Locate every uninfected red blood cell.
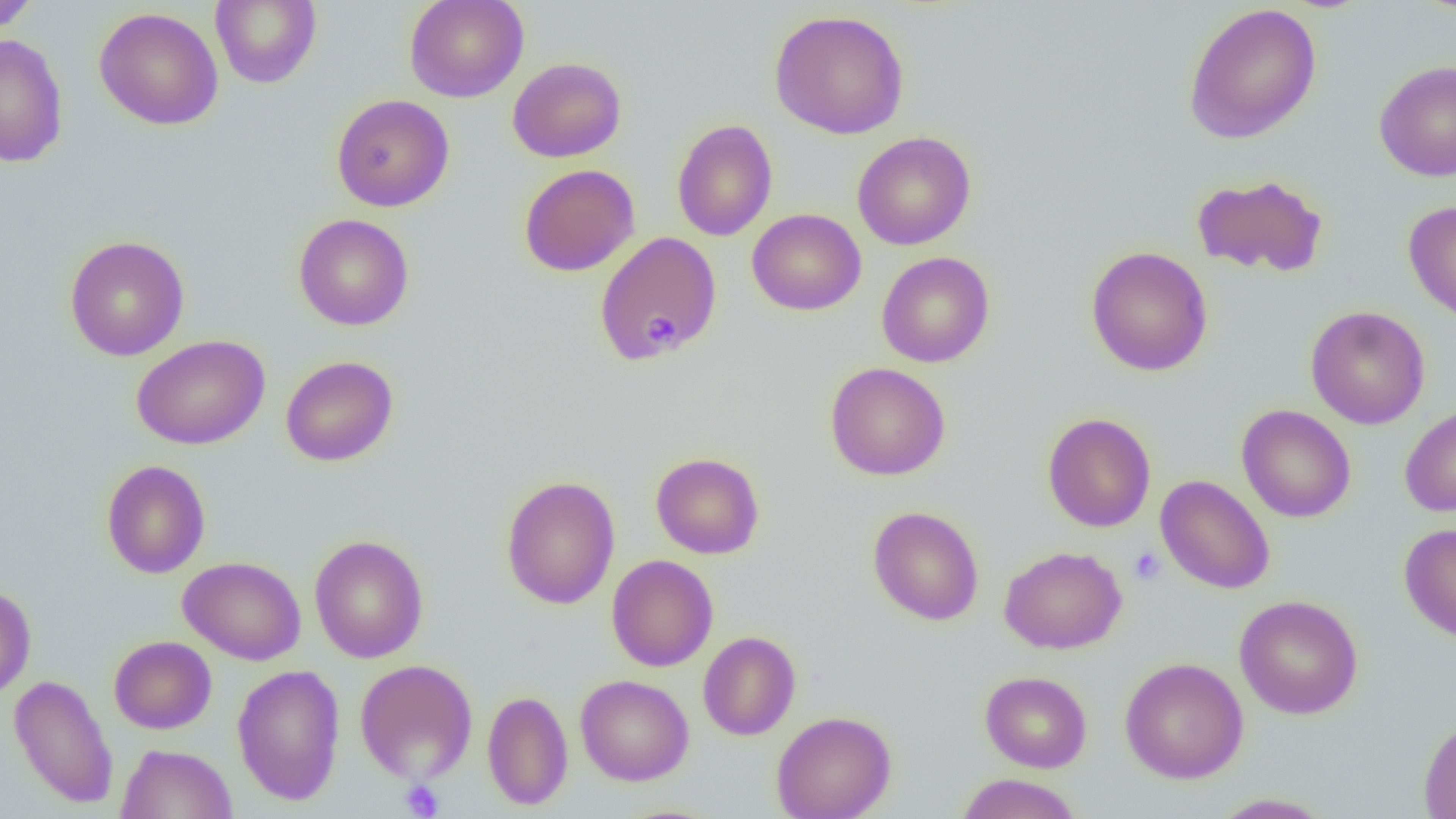
Approximate bounding boxes as [x1, y1, x2, y2] in pixels.
Uninfected red blood cells: [0, 0, 40, 34], [210, 0, 322, 88], [404, 0, 529, 102], [1414, 0, 1456, 16], [1183, 2, 1322, 144], [94, 7, 224, 131], [769, 9, 910, 139], [1, 34, 69, 167], [508, 57, 626, 163], [1374, 60, 1456, 182], [331, 95, 454, 212], [672, 119, 777, 241], [851, 131, 976, 250], [519, 164, 640, 277], [1191, 174, 1328, 278], [1403, 200, 1456, 324], [747, 209, 866, 315], [293, 213, 414, 331], [594, 233, 722, 364], [64, 235, 190, 361], [1085, 246, 1213, 377], [877, 251, 995, 368], [1305, 305, 1430, 430], [131, 334, 270, 450], [280, 355, 398, 466], [824, 362, 951, 480], [1399, 402, 1456, 518], [1236, 404, 1356, 523], [1042, 412, 1156, 532], [650, 452, 764, 559], [101, 460, 211, 578], [501, 475, 620, 609], [1156, 475, 1275, 595], [868, 506, 984, 625], [1399, 522, 1456, 642], [309, 534, 429, 664], [999, 545, 1127, 654], [606, 555, 718, 671], [178, 556, 306, 665], [0, 585, 36, 700], [1234, 594, 1363, 719], [698, 631, 801, 741], [109, 636, 216, 734], [1120, 656, 1249, 784], [354, 658, 478, 784], [232, 664, 345, 805], [980, 671, 1092, 773], [8, 673, 119, 809], [575, 674, 694, 786], [482, 689, 573, 810], [771, 710, 897, 819], [1418, 715, 1456, 819], [116, 743, 236, 819], [954, 773, 1083, 819], [1210, 793, 1334, 818].

Summary:
  - Platelet locations: [643, 317, 680, 351], [1128, 547, 1166, 585], [400, 779, 443, 818]
  - Slide-level diagnosis: no evidence of blood parasites
  - Field of view: one of a larger specimen
  - Preparation: thin blood smear
  - Modality: optical microscopy
  - Magnification: 1000x
  - Image size: 1456×819 pixels